Locate every Plasmodium malariae-infected red blood cell.
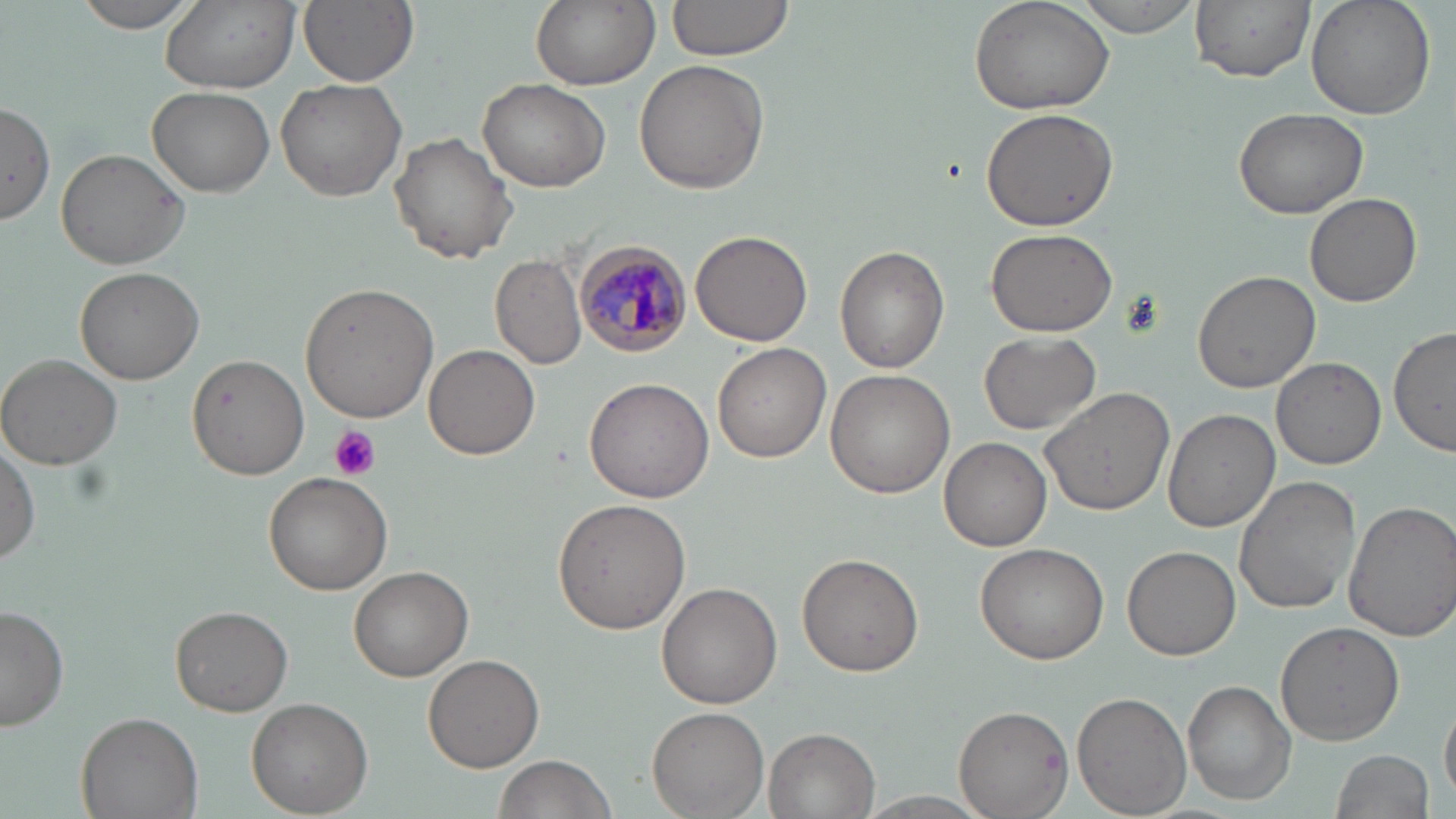
Approximate bounding boxes as named x1/y1/x2/y2 corners in pixels.
Plasmodium malariae-infected red blood cells: (x1=575, y1=242, x2=693, y2=357).

{
  "slide_level_diagnosis": "Plasmodium malariae",
  "field_of_view": "one of a larger specimen",
  "image_size": "1456×819 pixels",
  "uninfected_red_blood_cell_locations": "approximate bounding boxes as named x1/y1/x2/y2 corners in pixels: (x1=71, y1=0, x2=202, y2=33), (x1=158, y1=0, x2=301, y2=94), (x1=299, y1=0, x2=420, y2=87), (x1=529, y1=0, x2=659, y2=91), (x1=664, y1=0, x2=799, y2=62), (x1=968, y1=0, x2=1116, y2=117), (x1=1070, y1=0, x2=1206, y2=37), (x1=1191, y1=0, x2=1315, y2=83), (x1=1305, y1=0, x2=1437, y2=119), (x1=634, y1=60, x2=769, y2=194), (x1=476, y1=77, x2=610, y2=192), (x1=276, y1=80, x2=406, y2=202), (x1=149, y1=87, x2=275, y2=199), (x1=0, y1=105, x2=54, y2=227), (x1=979, y1=105, x2=1119, y2=231), (x1=1233, y1=107, x2=1369, y2=219), (x1=387, y1=133, x2=517, y2=264), (x1=56, y1=148, x2=189, y2=269), (x1=1305, y1=193, x2=1422, y2=308), (x1=985, y1=228, x2=1117, y2=336), (x1=691, y1=231, x2=813, y2=347), (x1=835, y1=247, x2=949, y2=374), (x1=490, y1=252, x2=588, y2=370), (x1=75, y1=267, x2=204, y2=384), (x1=1191, y1=270, x2=1320, y2=394), (x1=300, y1=281, x2=441, y2=421), (x1=1388, y1=325, x2=1455, y2=457), (x1=979, y1=331, x2=1102, y2=435), (x1=712, y1=343, x2=831, y2=463), (x1=422, y1=344, x2=540, y2=460), (x1=189, y1=354, x2=310, y2=479), (x1=0, y1=355, x2=127, y2=472), (x1=1271, y1=356, x2=1388, y2=470), (x1=824, y1=369, x2=952, y2=500), (x1=583, y1=376, x2=715, y2=505), (x1=1040, y1=387, x2=1175, y2=516), (x1=1165, y1=408, x2=1280, y2=533), (x1=938, y1=436, x2=1052, y2=551), (x1=0, y1=437, x2=39, y2=565), (x1=263, y1=471, x2=393, y2=594), (x1=1232, y1=476, x2=1360, y2=616), (x1=551, y1=499, x2=691, y2=634), (x1=1342, y1=500, x2=1456, y2=641), (x1=975, y1=543, x2=1110, y2=664), (x1=1121, y1=544, x2=1239, y2=660), (x1=797, y1=553, x2=925, y2=678), (x1=348, y1=564, x2=473, y2=680), (x1=657, y1=580, x2=783, y2=708), (x1=0, y1=604, x2=70, y2=733), (x1=169, y1=604, x2=293, y2=716), (x1=1275, y1=622, x2=1405, y2=746), (x1=421, y1=653, x2=546, y2=772), (x1=1183, y1=679, x2=1296, y2=806), (x1=1073, y1=692, x2=1191, y2=818), (x1=1440, y1=694, x2=1455, y2=808), (x1=247, y1=696, x2=374, y2=816), (x1=955, y1=704, x2=1073, y2=818), (x1=647, y1=706, x2=767, y2=819), (x1=76, y1=710, x2=203, y2=819), (x1=766, y1=728, x2=880, y2=817), (x1=1330, y1=749, x2=1435, y2=819), (x1=491, y1=756, x2=619, y2=819), (x1=848, y1=791, x2=1003, y2=819)",
  "modality": "light microscopy",
  "platelet_locations": "approximate bounding boxes as named x1/y1/x2/y2 corners in pixels: (x1=327, y1=426, x2=380, y2=481)",
  "stain": "May-Grünwald-Giemsa",
  "magnification": "1000x",
  "preparation": "thin blood film"
}